Identify the parasite.
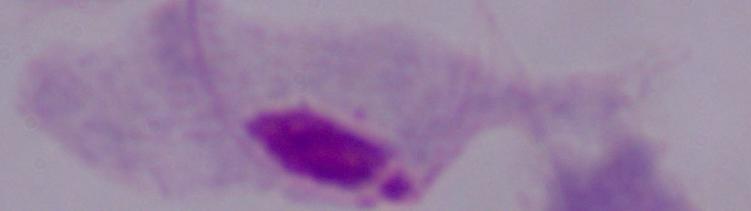
This is a trichomonad.

Captured at 1000x magnification. Micrograph.